Name the parasite shown.
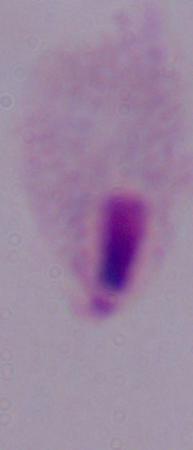
A trichomonad.

Summary:
  - Magnification: 1000x
  - Modality: photomicrograph